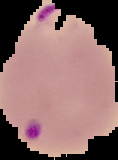

Summary:
  - Malaria status: parasitized
  - Preparation: thin blood smear
  - Image size: 118×160 pixels
  - Image type: segmented cell region with the area outside set to black